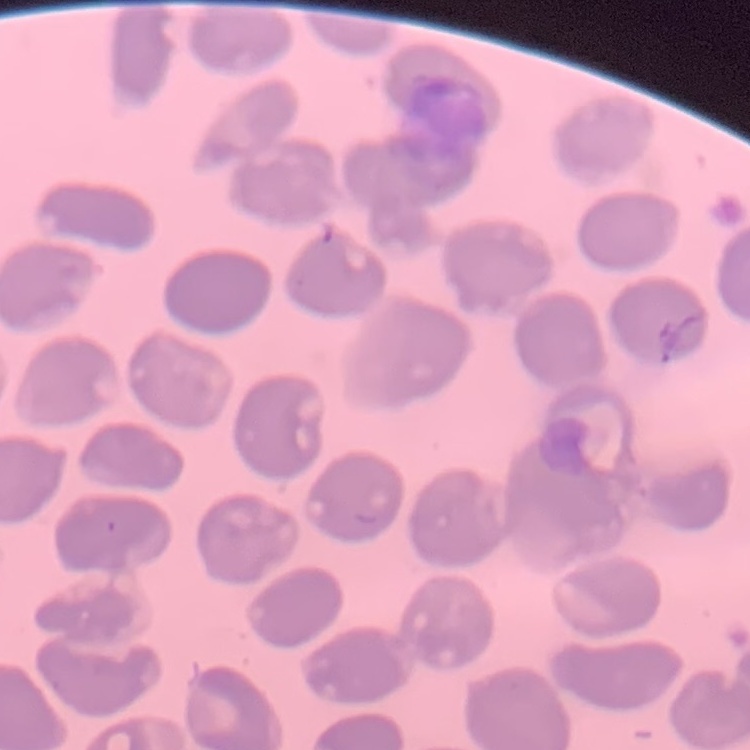 The erythrocytes show no rouleaux formation. Thin blood film. Field's or Giemsa stain. One tile cut from a larger photomicrograph.